Assess this cell for malaria.
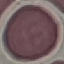
Uninfected.

Photographed with a smartphone camera at the microscope eyepiece. Giemsa stain. Cell patch, automatically extracted from a larger field of view and resized to 64 × 64 pixels. Thin blood film.